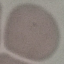 Malaria status: uninfected. Giemsa stain. Photographed with a smartphone camera at the microscope eyepiece. Thin smear of blood. Cell patch, automatically extracted from a larger field of view and resized to 64 × 64 pixels.